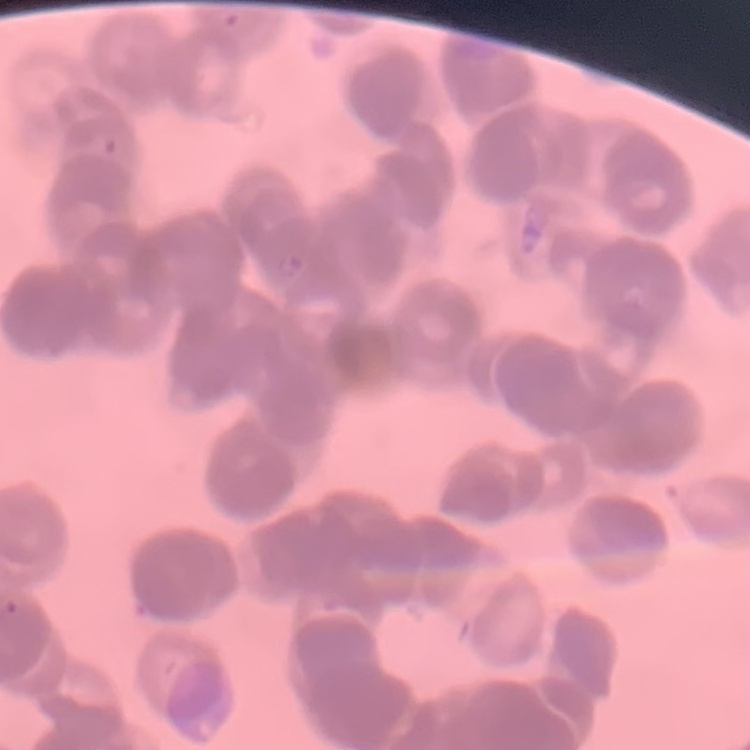
The red blood cells show rouleaux formation. Thin peripheral smear. One tile cut from a larger photomicrograph. Field's or Giemsa stain.